Classify this cell by malaria status.
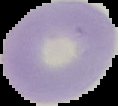
It is uninfected.

preparation: thin blood film
image_size: 118×106 pixels
image_type: cell region segmented out of the field of view; surrounding area masked to black